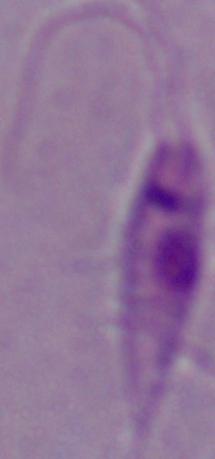
Micrograph. 1000x magnification. A Leishmania parasite is seen.